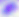

identification = Toxoplasma gondii
modality = micrograph
magnification = 400x